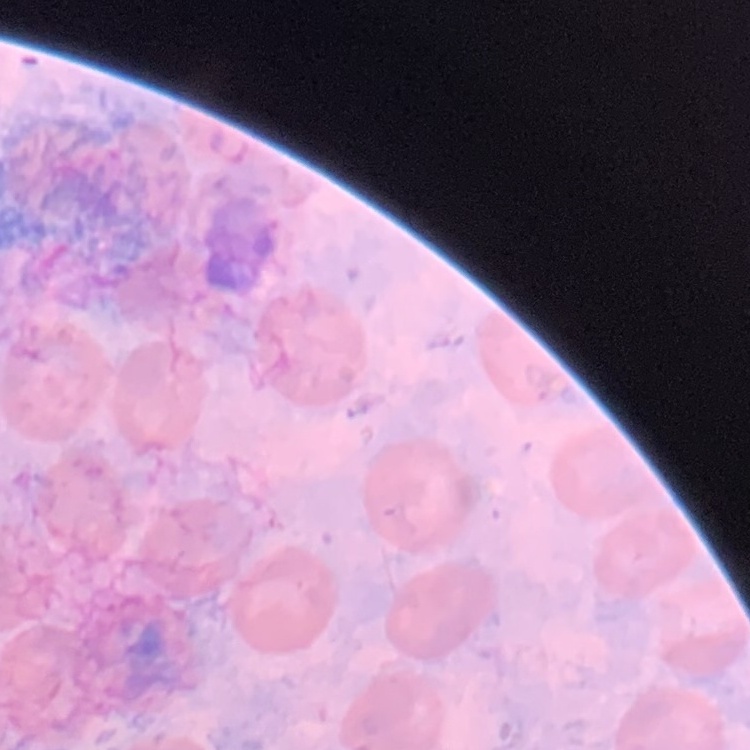
{
  "red_blood_cell_morphology": "no rouleaux formation",
  "stain": "Field's or Giemsa",
  "preparation": "thin blood film",
  "image_type": "one tile cut from a larger photomicrograph"
}